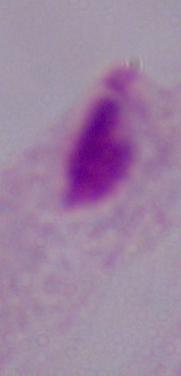

Summary:
  - Modality: photomicrograph
  - Identification: trichomonad
  - Magnification: 1000x